Classify this cell by malaria status.
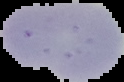
Uninfected.

image size = 124×82 pixels
image type = segmented cell region with the area outside set to black
preparation = thin blood smear